Assess this cell for malaria.
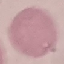

Uninfected.

Summary:
  - Preparation: thin blood film
  - Image type: automatically extracted cell patch, resized to 64 × 64 pixels
  - Stain: Giemsa
  - Capture: smartphone through the microscope eyepiece